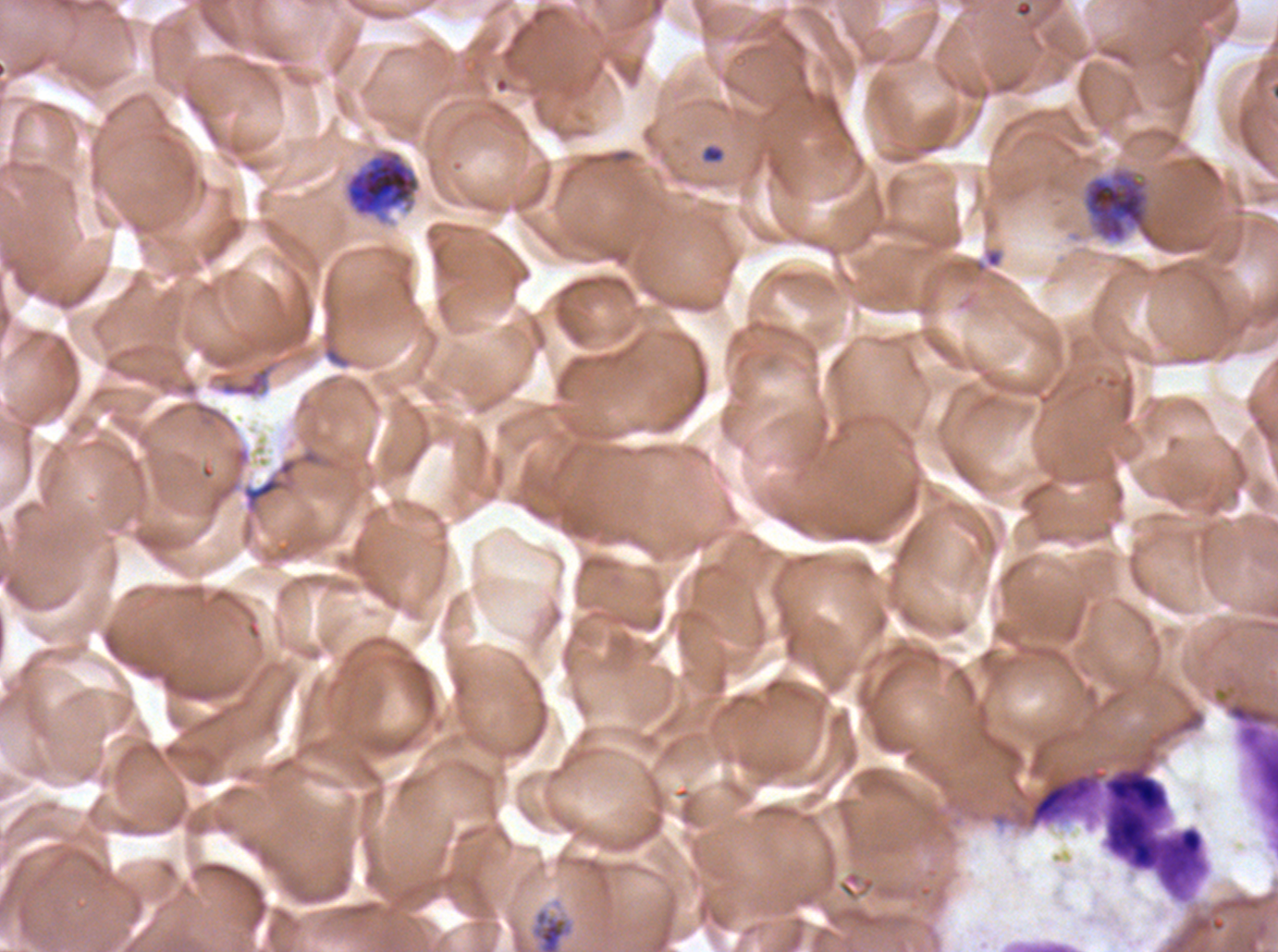
Approximate bounding boxes as [x1, y1, x2, y2] in pixels. Ring locations: [701, 144, 725, 164]. Mid trophozoite locations: [529, 907, 575, 951]. Leukocyte locations: [1025, 746, 1210, 903]. Segmenter locations: [342, 147, 422, 226], [1083, 169, 1159, 246]. Thin blood smear. A sub-image separated from a larger composite. Giemsa stain. Plasmodium falciparum cultured ex vivo for 24 to 48 hours, from a patient in The Gambia. Life-cycle stages observed: ring, mid trophozoite, segmenter. Image is 1278×952 pixels.